State which parasite is depicted.
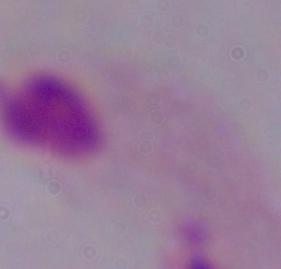
A trichomonad.

magnification: 1000x
modality: micrograph